Point out every malaria parasite and every leukocyte.
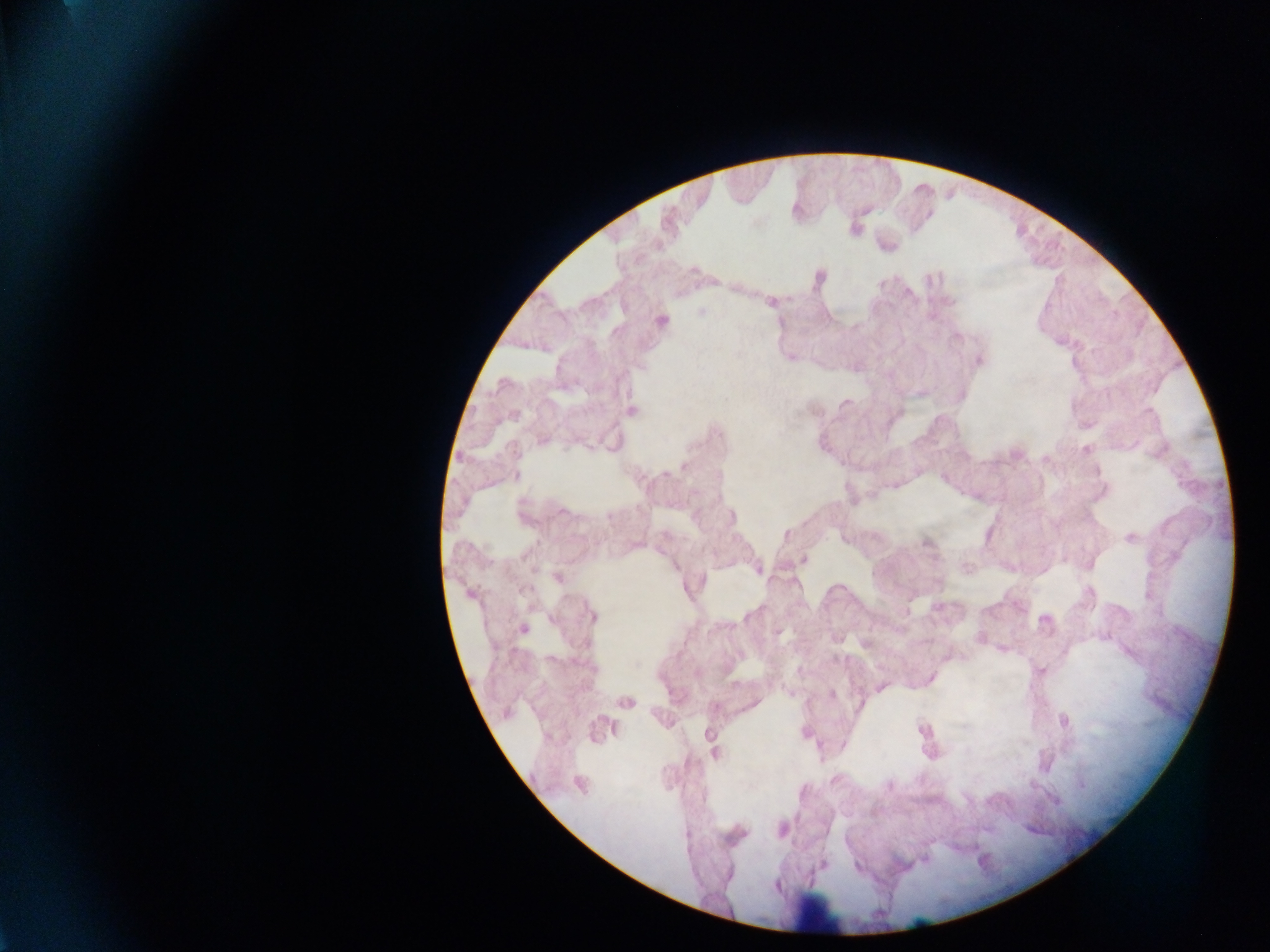

Approximate centers as x y in pixels.
Malaria parasites: 558 578; 523 628.
Leukocytes: 820 912.

Mobile-phone photograph taken through the microscope. Image is 1270×952 pixels. Thick blood smear. Collected in Ghana. Single field of view.